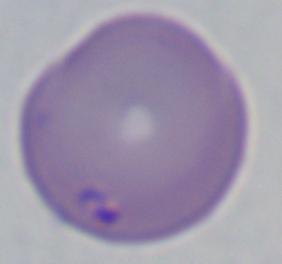

Captured at 1000x magnification. Photomicrograph. A Babesia parasite is shown.